Comment on the morphology of the red blood cells.
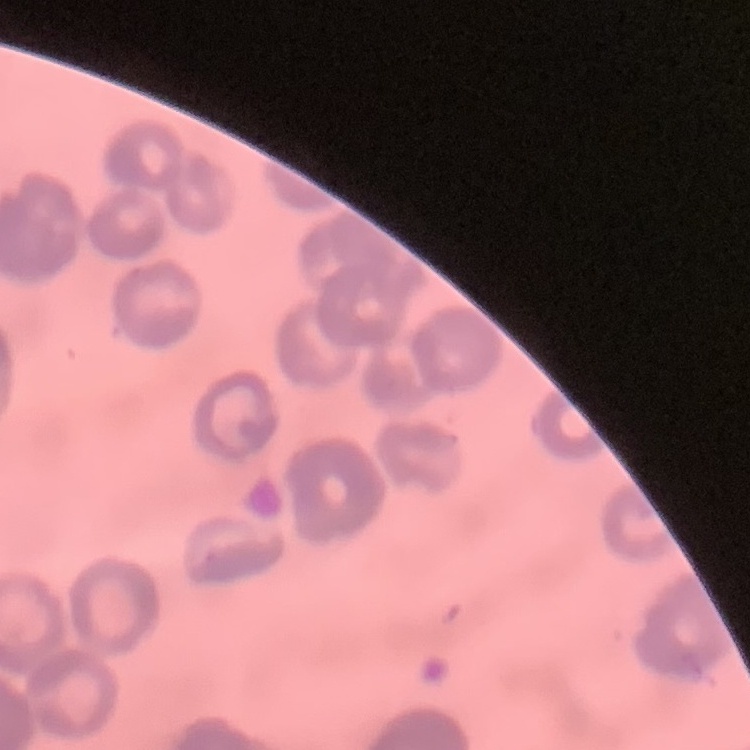
Rouleaux formation.

image type = square crop of a larger photomicrograph
preparation = thin peripheral smear
stain = Field's or Giemsa